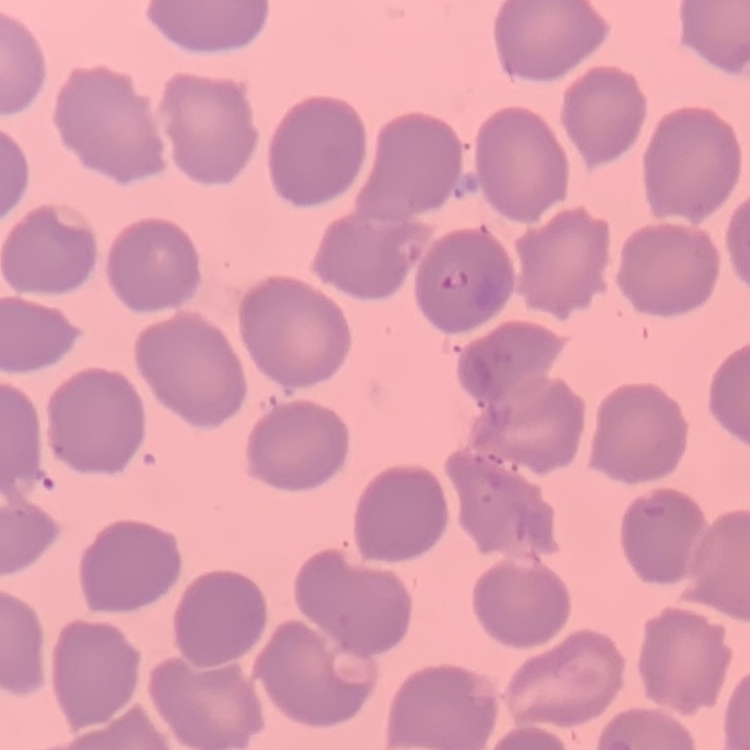
Summary:
  - Red blood cell morphology: no rouleaux formation
  - Stain: Field's or Giemsa
  - Preparation: thin peripheral smear
  - Image type: square crop of a larger photomicrograph